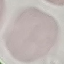

Malaria status: uninfected. Cell patch, automatically extracted from a larger field of view and resized to 64 × 64 pixels. Thin smear of blood. Giemsa-stained preparation. Photographed with a smartphone camera at the microscope eyepiece.